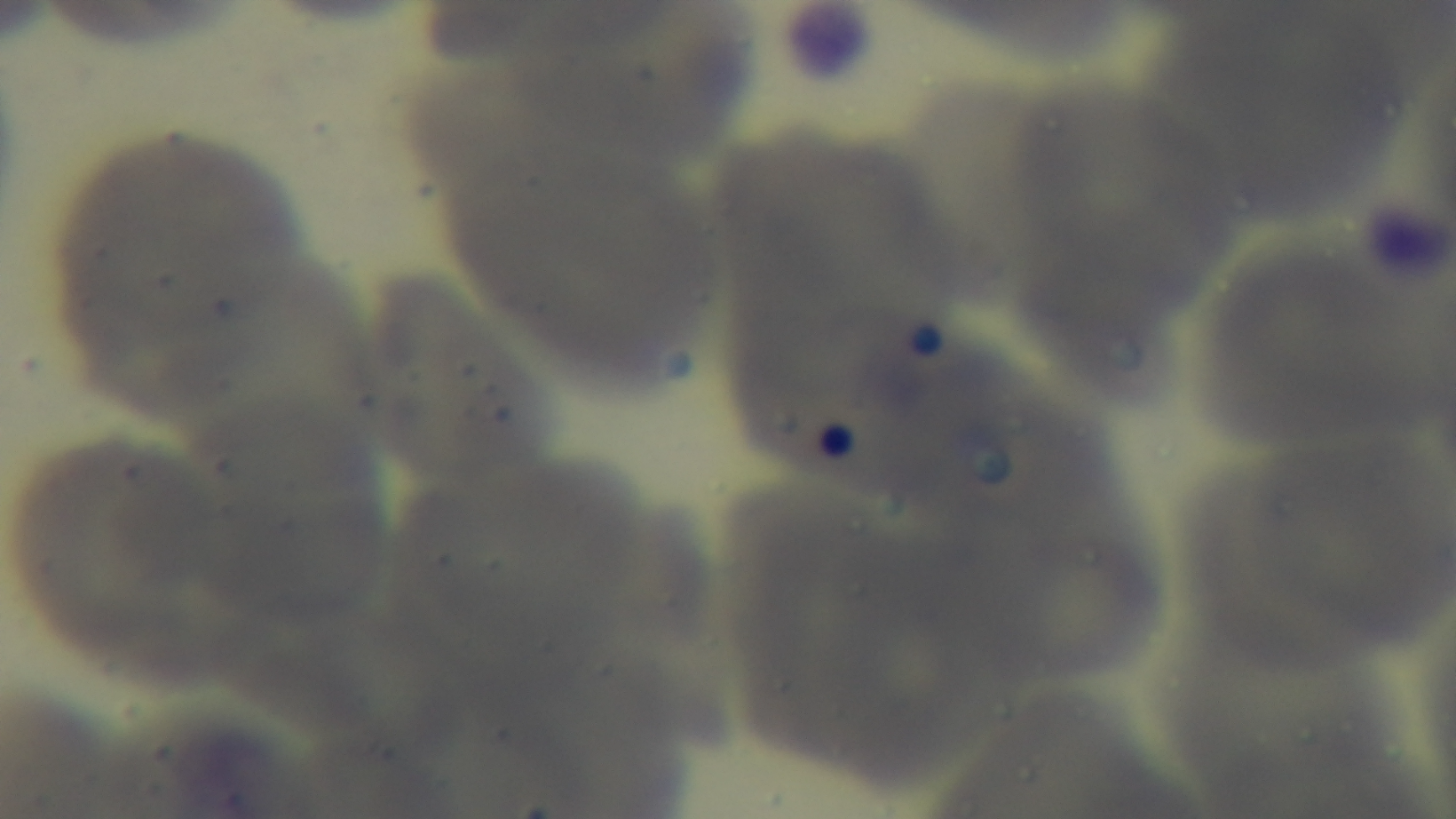

Captured with a mounted 4K digital camera. Photomicrograph. Malaria status: negative. Single field of view. 100x oil-immersion objective. Preparation: thin blood film. Giemsa stain.